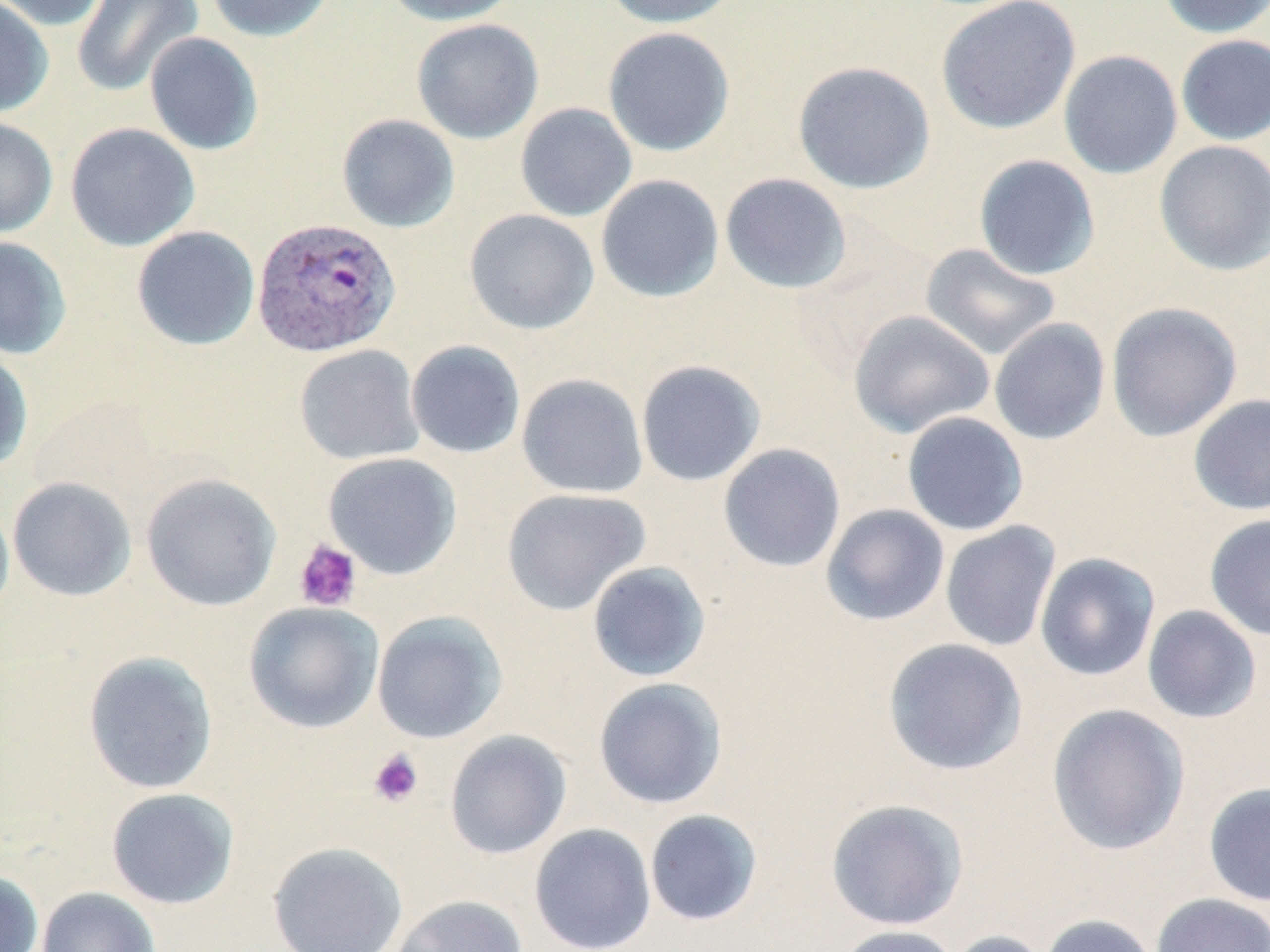

Approximate bounding boxes as named x1/y1/x2/y2 corners in pixels. Plasmodium vivax-infected red blood cell locations: (x1=252, y1=216, x2=401, y2=358). Uninfected red blood cell locations: (x1=0, y1=0, x2=110, y2=31), (x1=72, y1=0, x2=204, y2=97), (x1=204, y1=0, x2=335, y2=42), (x1=381, y1=0, x2=521, y2=26), (x1=603, y1=0, x2=740, y2=28), (x1=935, y1=0, x2=1081, y2=134), (x1=1156, y1=0, x2=1270, y2=38), (x1=0, y1=1, x2=54, y2=118), (x1=412, y1=19, x2=544, y2=144), (x1=603, y1=27, x2=735, y2=156), (x1=144, y1=32, x2=264, y2=155), (x1=1175, y1=34, x2=1270, y2=146), (x1=1058, y1=50, x2=1183, y2=179), (x1=792, y1=60, x2=936, y2=194), (x1=515, y1=102, x2=637, y2=222), (x1=336, y1=113, x2=460, y2=233), (x1=0, y1=116, x2=58, y2=239), (x1=64, y1=122, x2=200, y2=251), (x1=1154, y1=140, x2=1270, y2=276), (x1=973, y1=155, x2=1100, y2=280), (x1=720, y1=173, x2=852, y2=294), (x1=595, y1=174, x2=724, y2=303), (x1=464, y1=208, x2=599, y2=335), (x1=131, y1=225, x2=260, y2=351), (x1=0, y1=236, x2=72, y2=360), (x1=920, y1=243, x2=1061, y2=360), (x1=1106, y1=302, x2=1242, y2=442), (x1=848, y1=309, x2=995, y2=439), (x1=989, y1=318, x2=1111, y2=445), (x1=405, y1=340, x2=526, y2=459), (x1=294, y1=344, x2=424, y2=465), (x1=0, y1=347, x2=34, y2=474), (x1=635, y1=359, x2=767, y2=487), (x1=516, y1=372, x2=648, y2=499), (x1=1188, y1=394, x2=1270, y2=515), (x1=901, y1=411, x2=1029, y2=536), (x1=718, y1=443, x2=846, y2=572), (x1=323, y1=452, x2=462, y2=579), (x1=141, y1=473, x2=282, y2=612), (x1=7, y1=477, x2=137, y2=602), (x1=501, y1=488, x2=651, y2=616), (x1=0, y1=497, x2=14, y2=621), (x1=820, y1=504, x2=950, y2=626), (x1=1205, y1=512, x2=1270, y2=641), (x1=940, y1=521, x2=1061, y2=652), (x1=1034, y1=551, x2=1160, y2=681), (x1=586, y1=560, x2=711, y2=682), (x1=243, y1=601, x2=385, y2=733), (x1=1142, y1=605, x2=1262, y2=724), (x1=371, y1=611, x2=508, y2=744), (x1=882, y1=637, x2=1028, y2=776), (x1=82, y1=651, x2=219, y2=794), (x1=593, y1=677, x2=728, y2=809), (x1=1046, y1=703, x2=1190, y2=856), (x1=444, y1=729, x2=572, y2=860), (x1=1203, y1=782, x2=1270, y2=907), (x1=106, y1=788, x2=240, y2=909), (x1=825, y1=798, x2=968, y2=931), (x1=644, y1=809, x2=764, y2=927), (x1=528, y1=823, x2=656, y2=952), (x1=267, y1=841, x2=408, y2=952), (x1=0, y1=870, x2=44, y2=952), (x1=36, y1=887, x2=160, y2=952), (x1=1151, y1=893, x2=1270, y2=952), (x1=390, y1=894, x2=528, y2=952), (x1=1040, y1=913, x2=1160, y2=952), (x1=834, y1=924, x2=961, y2=952), (x1=941, y1=930, x2=1054, y2=952). Platelet locations: (x1=293, y1=539, x2=362, y2=612), (x1=367, y1=749, x2=424, y2=807). Slide-level diagnosis: Plasmodium vivax. Thin blood smear. One field of a larger specimen. May-Grünwald-Giemsa-stained preparation. Image is 1270×952 pixels. Light microscopy. 1000x magnification.